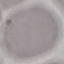
Result: negative for malaria parasites. Thin smear of blood. Acquired by smartphone through the microscope eyepiece. Automatically extracted cell patch, resized to 64 × 64 pixels. Giemsa stain.